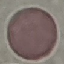

Summary:
  - Result: negative for malaria parasites
  - Stain: Giemsa
  - Image type: cell patch, automatically extracted from a larger field of view and resized to 64 × 64 pixels
  - Preparation: thin smear
  - Capture: smartphone through the microscope eyepiece